Assess the morphology of the erythrocytes.
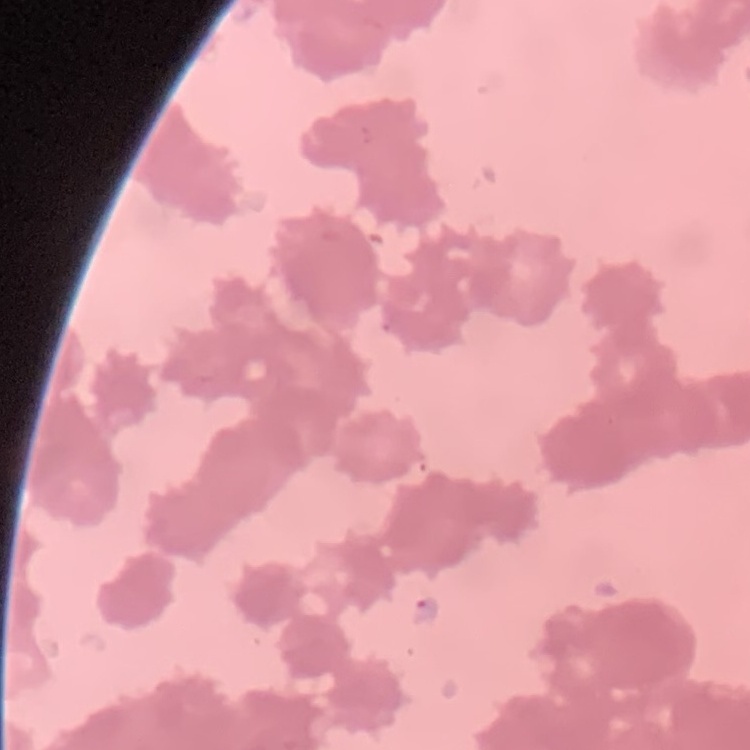
Rouleaux formation.

{
  "image_type": "square crop of a larger photomicrograph",
  "stain": "Field's or Giemsa",
  "preparation": "thin peripheral smear"
}